Identify the cell.
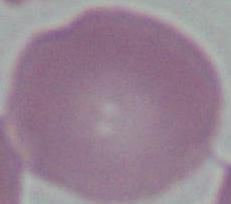

This is an erythrocyte.

1000x magnification. Photomicrograph.